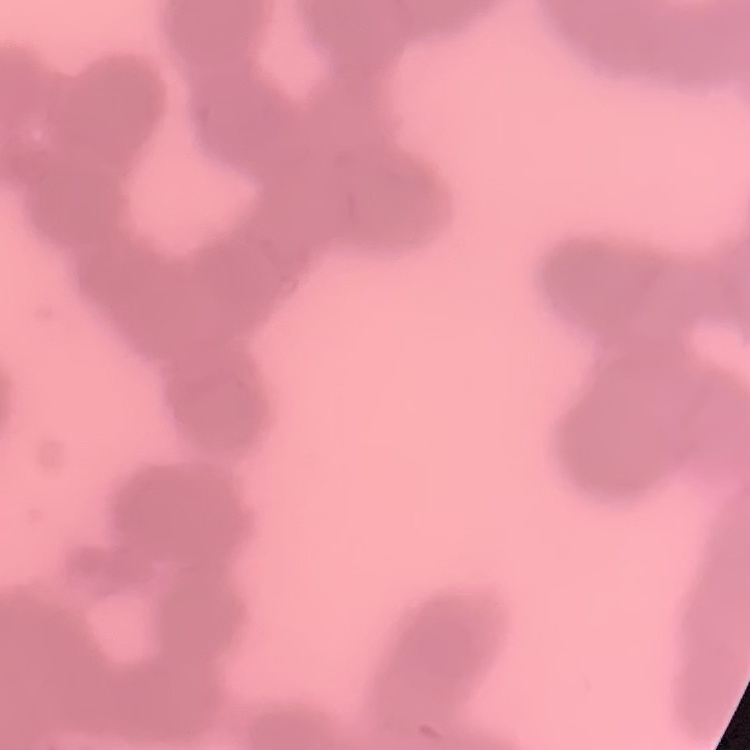
The red blood cells exhibit rouleaux formation. One tile cut from a larger photomicrograph. Stained with either Field's or Giemsa. Thin blood film.